Locate platelets.
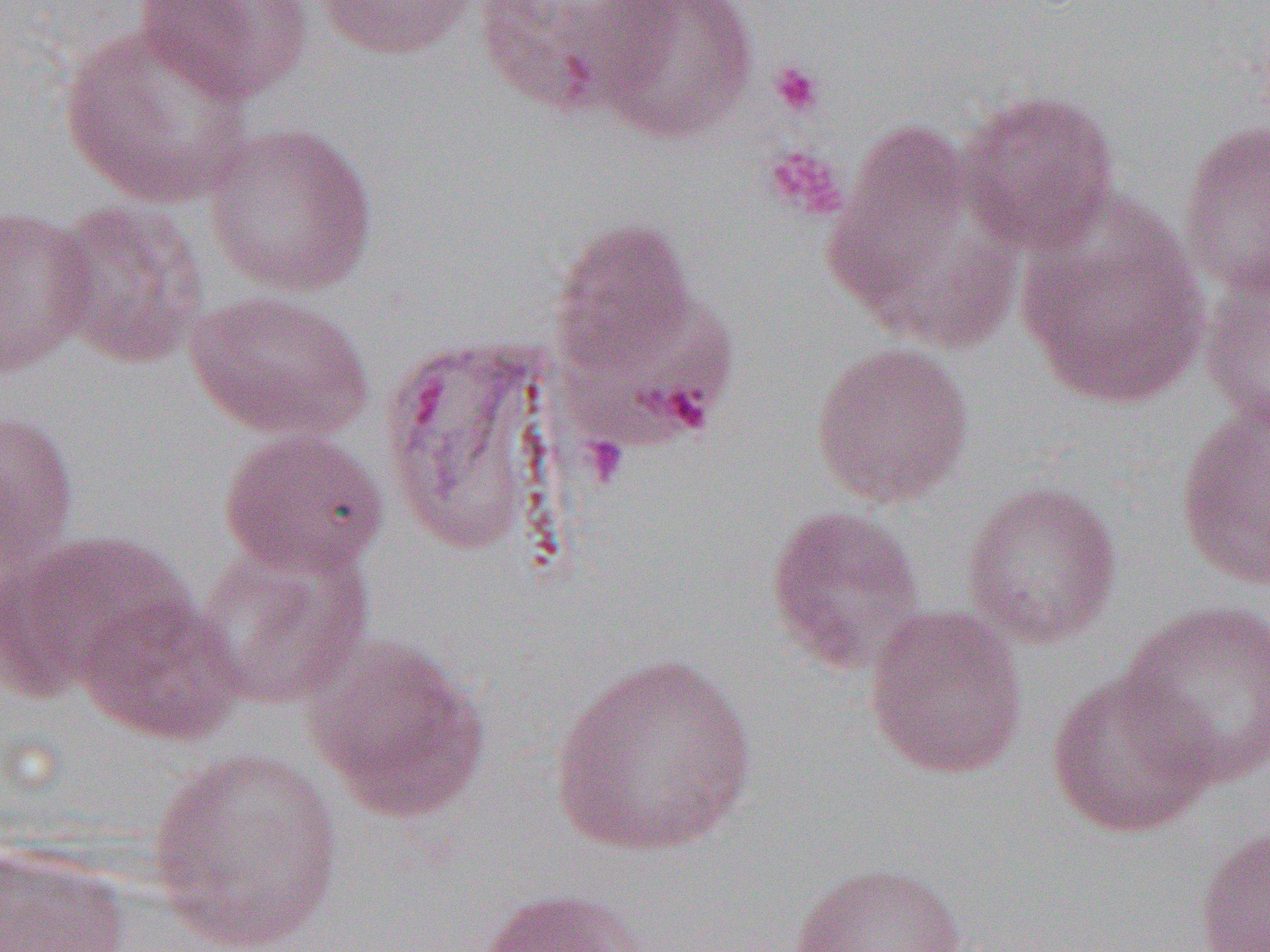

Approximate bounding boxes as (x1,y1)-(x2,y2) corner pairs in pixels.
Platelets: (769,62)-(825,117), (763,145)-(849,221), (581,434)-(630,487).

slide_level_diagnosis: Plasmodium vivax
image_size: 1270×952 pixels
field_of_view: single
modality: light microscopy
magnification: 1000x
preparation: thin blood film
uninfected_red_blood_cell_locations: 'approximate bounding boxes as (x1,y1)-(x2,y2) corner pairs in pixels: (134,0)-(313,103), (317,0)-(478,60), (472,0)-(659,118), (589,0)-(759,145), (59,20)-(254,209), (955,89)-(1122,253), (1179,119)-(1270,299), (203,121)-(379,297), (826,121)-(1013,348), (1015,196)-(1211,410), (45,199)-(211,369), (0,204)-(97,378), (551,217)-(699,374), (1200,264)-(1270,429), (186,292)-(374,440), (368,327)-(590,571), (811,339)-(974,509), (1174,402)-(1270,592), (0,409)-(80,575), (218,428)-(388,578), (961,480)-(1124,650), (765,504)-(927,674), (1,529)-(195,699), (195,538)-(374,711), (75,595)-(247,746), (1117,598)-(1270,790), (863,604)-(1029,779), (303,636)-(490,822), (547,653)-(760,859), (1045,668)-(1220,841), (146,747)-(347,951), (1194,821)-(1270,952), (0,842)-(134,952), (788,861)-(967,952), (478,887)-(650,952)'